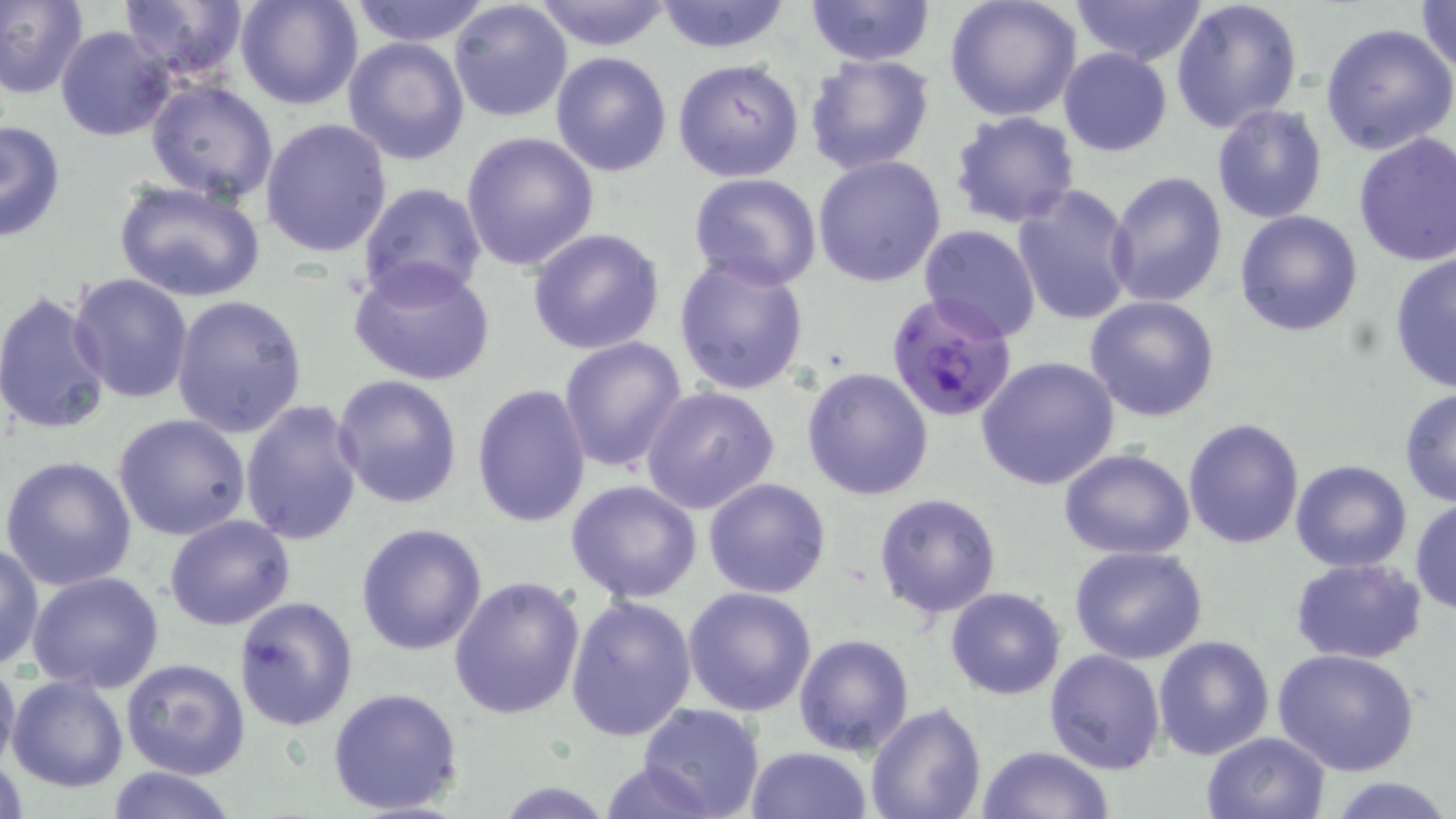

Summary:
  - Coordinate format: approximate bounding boxes as [x1, y1, x2, y2] in pixels
  - Plasmodium falciparum-infected red blood cell locations: [885, 291, 1018, 421]
  - Uninfected red blood cell locations: [0, 0, 88, 100], [118, 0, 252, 82], [237, 0, 363, 109], [347, 0, 492, 46], [531, 0, 673, 51], [652, 0, 794, 54], [803, 0, 935, 66], [942, 0, 1083, 120], [1070, 0, 1207, 67], [1170, 0, 1304, 133], [448, 1, 574, 123], [1411, 2, 1456, 77], [1320, 23, 1456, 157], [54, 26, 176, 143], [342, 35, 471, 165], [1058, 47, 1173, 157], [551, 51, 672, 177], [803, 53, 934, 175], [672, 57, 805, 183], [144, 78, 280, 205], [1211, 104, 1327, 223], [949, 110, 1080, 229], [259, 117, 393, 257], [0, 119, 65, 244], [1352, 131, 1456, 268], [461, 132, 599, 272], [812, 154, 948, 288], [1104, 169, 1229, 309], [688, 173, 823, 292], [113, 178, 266, 304], [358, 181, 488, 304], [1012, 184, 1139, 326], [1234, 210, 1363, 337], [916, 225, 1043, 343], [527, 228, 665, 355], [673, 254, 809, 397], [1388, 254, 1456, 395], [349, 260, 497, 388], [68, 273, 194, 403], [0, 290, 115, 438], [171, 294, 308, 438], [1083, 295, 1221, 422], [558, 335, 688, 475], [976, 355, 1119, 490], [801, 367, 935, 501], [331, 374, 462, 509], [472, 383, 593, 527], [640, 385, 779, 513], [1399, 387, 1456, 507], [239, 399, 365, 546], [113, 414, 254, 541], [1183, 417, 1305, 550], [1059, 447, 1197, 560], [1, 455, 138, 592], [1290, 459, 1413, 571], [703, 477, 833, 599], [566, 481, 703, 604], [872, 492, 1003, 619], [1410, 498, 1456, 616], [164, 514, 295, 630], [355, 523, 488, 655], [0, 541, 44, 671], [1068, 546, 1209, 663], [1289, 557, 1426, 664], [25, 571, 166, 695], [448, 576, 588, 723], [684, 585, 818, 717], [944, 587, 1066, 699], [232, 596, 358, 731], [566, 596, 698, 742], [793, 633, 915, 756], [1152, 634, 1275, 759], [1274, 647, 1421, 776], [1044, 648, 1165, 774], [0, 654, 21, 781], [120, 658, 251, 780], [7, 674, 128, 793], [326, 686, 464, 817], [637, 703, 766, 819], [864, 703, 986, 819], [1200, 731, 1331, 819], [745, 745, 872, 819], [977, 745, 1112, 819], [595, 759, 719, 819], [100, 765, 241, 819], [1334, 778, 1450, 817], [494, 781, 615, 816]
  - Slide-level diagnosis: Plasmodium falciparum
  - Stain: May-Grünwald-Giemsa
  - Modality: light microscopy
  - Magnification: 1000x
  - Field of view: single
  - Preparation: thin blood film
  - Image size: 1456×819 pixels